Locate every uninfected red blood cell.
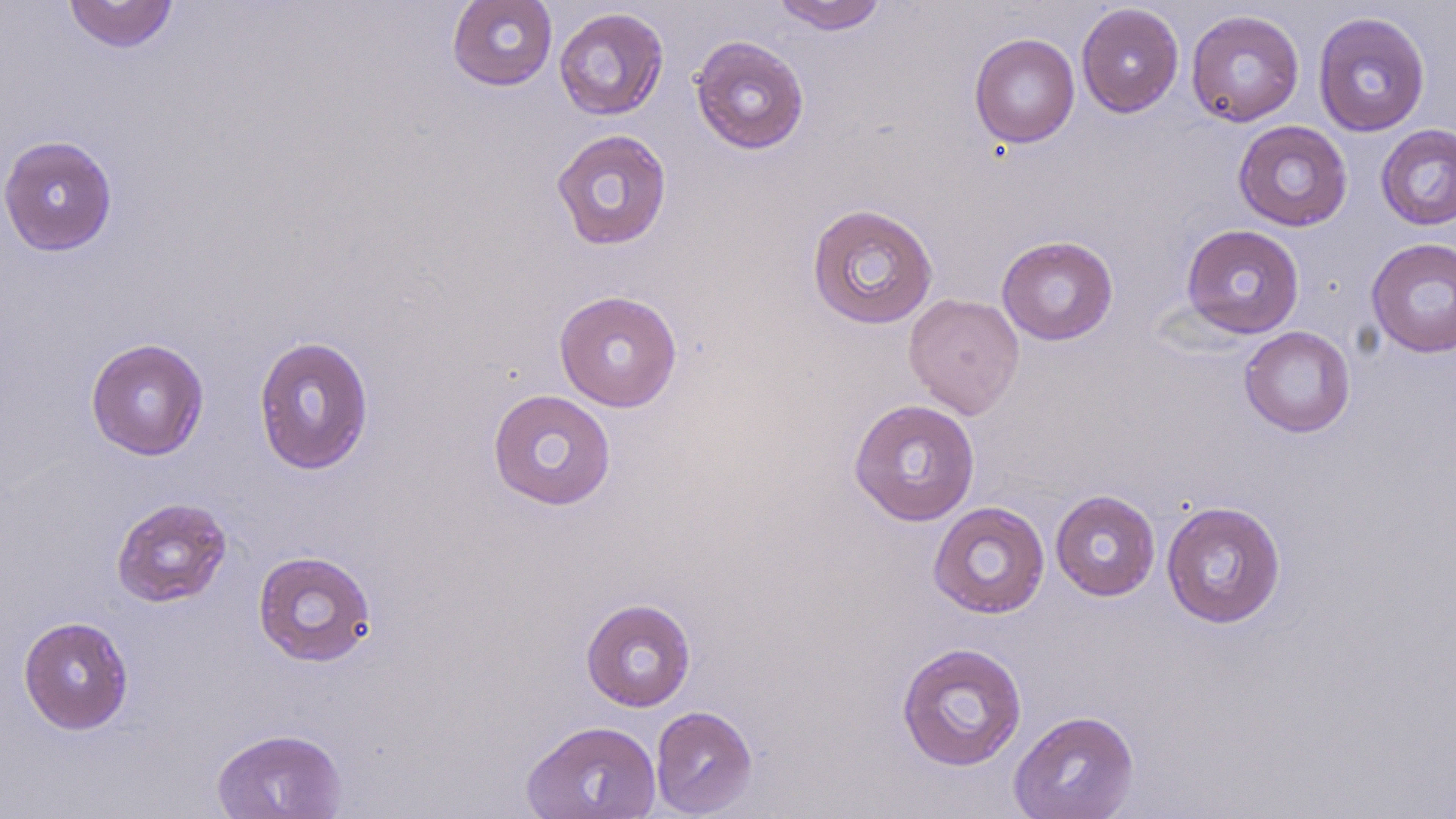
Approximate bounding boxes as (x1, y1, x2, y2) in pixels.
Uninfected red blood cells: (63, 0, 179, 53), (447, 0, 558, 91), (772, 0, 888, 34), (1076, 3, 1184, 117), (553, 7, 669, 121), (1186, 9, 1304, 127), (1313, 11, 1431, 137), (969, 33, 1080, 148), (689, 34, 810, 154), (1233, 120, 1352, 231), (1375, 124, 1456, 231), (550, 128, 672, 250), (0, 135, 118, 256), (806, 203, 939, 329), (1180, 224, 1305, 339), (997, 235, 1118, 345), (1366, 237, 1456, 358), (553, 290, 683, 412), (903, 292, 1024, 419), (1239, 326, 1355, 437), (253, 335, 375, 475), (85, 337, 209, 460), (487, 388, 617, 510), (848, 398, 981, 526), (1050, 489, 1160, 601), (111, 496, 232, 608), (1161, 500, 1287, 628), (927, 501, 1050, 619), (252, 550, 378, 667), (581, 598, 697, 711), (18, 615, 134, 734), (896, 641, 1028, 772), (650, 705, 758, 817), (1009, 709, 1140, 819), (521, 719, 662, 818), (211, 727, 347, 819).

slide-level diagnosis = no evidence of blood parasites
modality = light microscopy
magnification = 1000x
field of view = one of a larger specimen
image size = 1456×819 pixels
stain = May-Grünwald-Giemsa
preparation = thin blood film